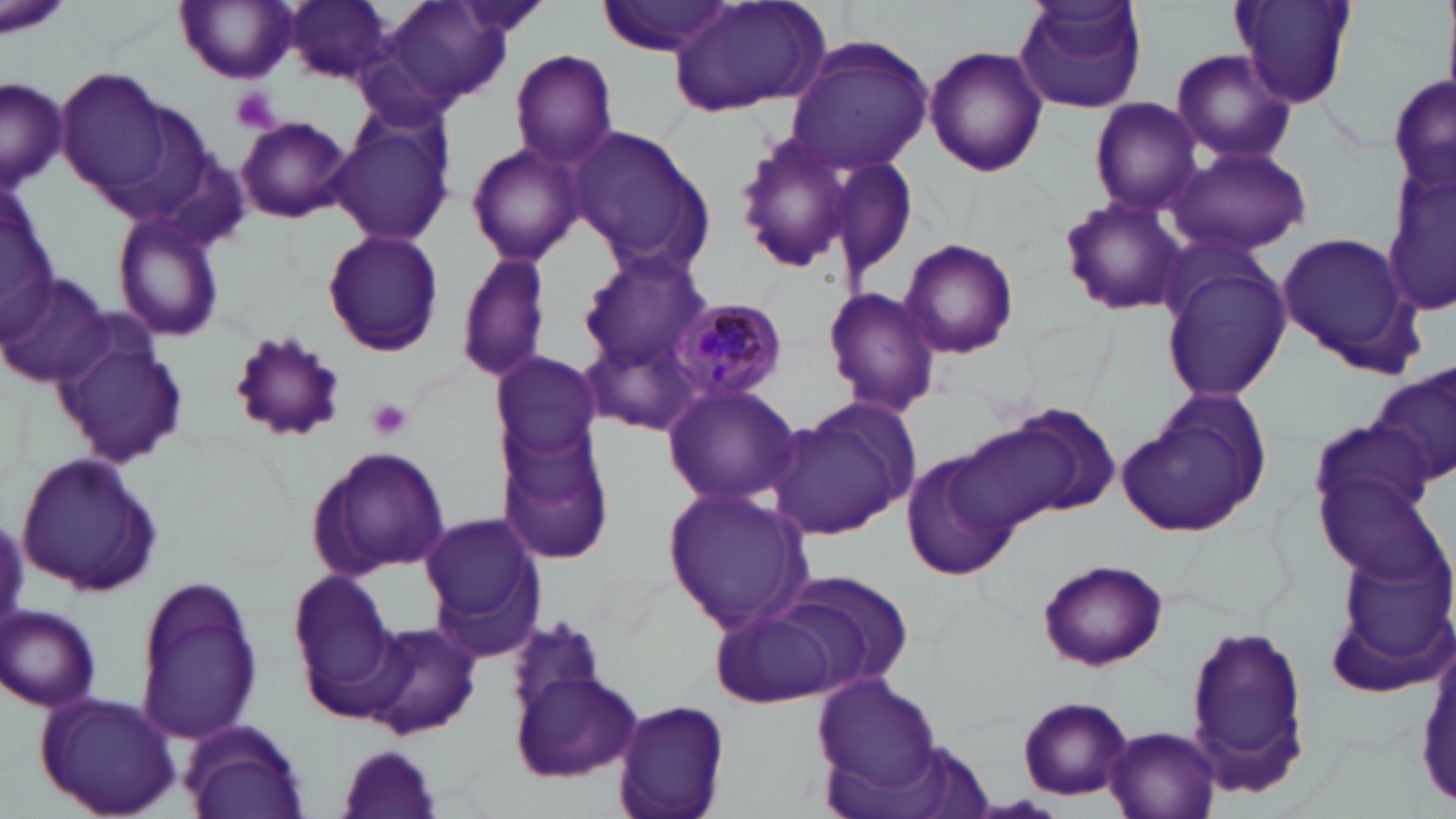
Summary:
  - Coordinate format: approximate bounding boxes as (x1,y1)-(x2,y2) corner pairs in pixels
  - Uninfected red blood cell locations: (1,0)-(72,40), (287,0)-(399,82), (451,0)-(557,38), (1012,0)-(1150,113), (1229,0)-(1356,109), (176,1)-(301,83), (383,1)-(513,106), (597,1)-(739,56), (666,2)-(831,116), (782,36)-(934,175), (925,45)-(1048,177), (510,48)-(618,169), (1169,48)-(1300,167), (56,70)-(176,197), (1389,72)-(1454,197), (1,77)-(66,191), (1089,99)-(1204,214), (328,114)-(454,247), (236,116)-(353,222), (569,126)-(714,275), (732,128)-(858,273), (467,140)-(588,263), (1168,144)-(1312,256), (1384,154)-(1456,321), (824,155)-(918,285), (0,182)-(55,335), (1058,194)-(1189,316), (113,211)-(226,344), (321,228)-(445,358), (1274,229)-(1426,376), (900,240)-(1020,359), (458,250)-(551,384), (579,254)-(708,367), (1161,257)-(1290,404), (0,274)-(112,385), (821,286)-(943,417), (581,318)-(706,435), (53,326)-(190,473), (224,329)-(347,444), (489,354)-(602,464), (1368,367)-(1455,492), (662,383)-(803,508), (1124,390)-(1271,534), (762,396)-(917,542), (981,402)-(1122,524), (1307,416)-(1434,530), (496,426)-(616,565), (307,444)-(449,578), (900,448)-(1020,585), (17,450)-(162,598), (1318,476)-(1449,588), (663,485)-(814,634), (421,513)-(546,655), (1330,549)-(1456,682), (1038,558)-(1168,671), (756,568)-(917,700), (285,573)-(402,721), (133,579)-(262,746), (3,604)-(101,711), (710,607)-(842,707), (503,615)-(615,726), (1182,620)-(1312,797), (362,621)-(481,742), (508,669)-(646,782), (808,672)-(943,796), (34,690)-(185,818), (1017,695)-(1134,800), (614,699)-(731,819), (182,720)-(308,819), (1102,725)-(1220,819), (337,745)-(446,819)
  - Plasmodium malariae-infected red blood cell locations: (669,296)-(790,407)
  - White blood cell locations: (14,451)-(166,598)
  - Platelet locations: (230,87)-(282,134), (366,397)-(413,442)
  - Slide-level diagnosis: Plasmodium malariae
  - Image size: 1456×819 pixels
  - Stain: May-Grünwald-Giemsa
  - Field of view: one of a larger specimen
  - Modality: light microscopy
  - Magnification: 1000x
  - Preparation: thin blood film